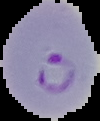
image type = segmented cell region with the area outside set to black
image size = 100×121 pixels
preparation = thin blood film
malaria status = parasitized